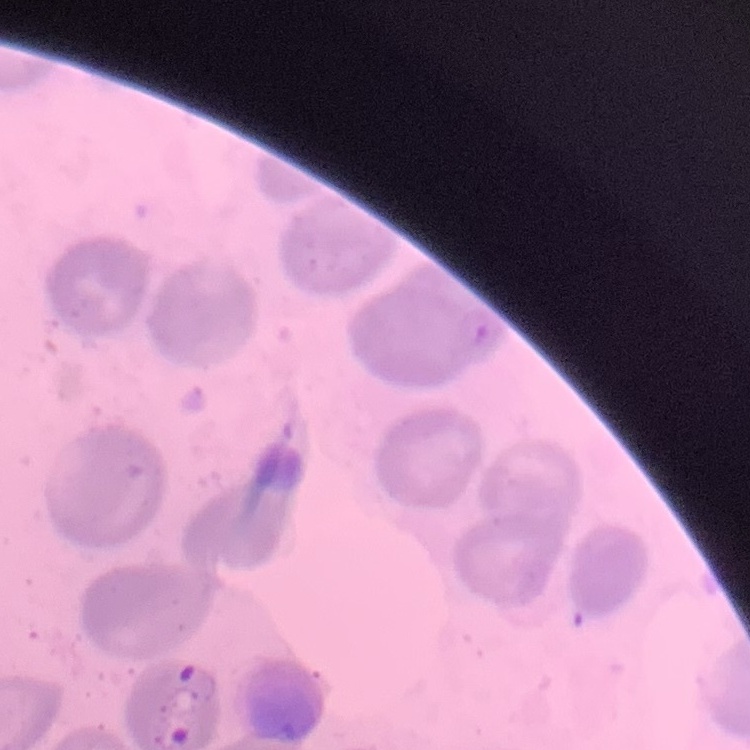

The erythrocytes show no rouleaux formation. One tile cut from a larger photomicrograph. Stained with either Field's or Giemsa. Thin blood film.